Outline each blood parasite and name the species.
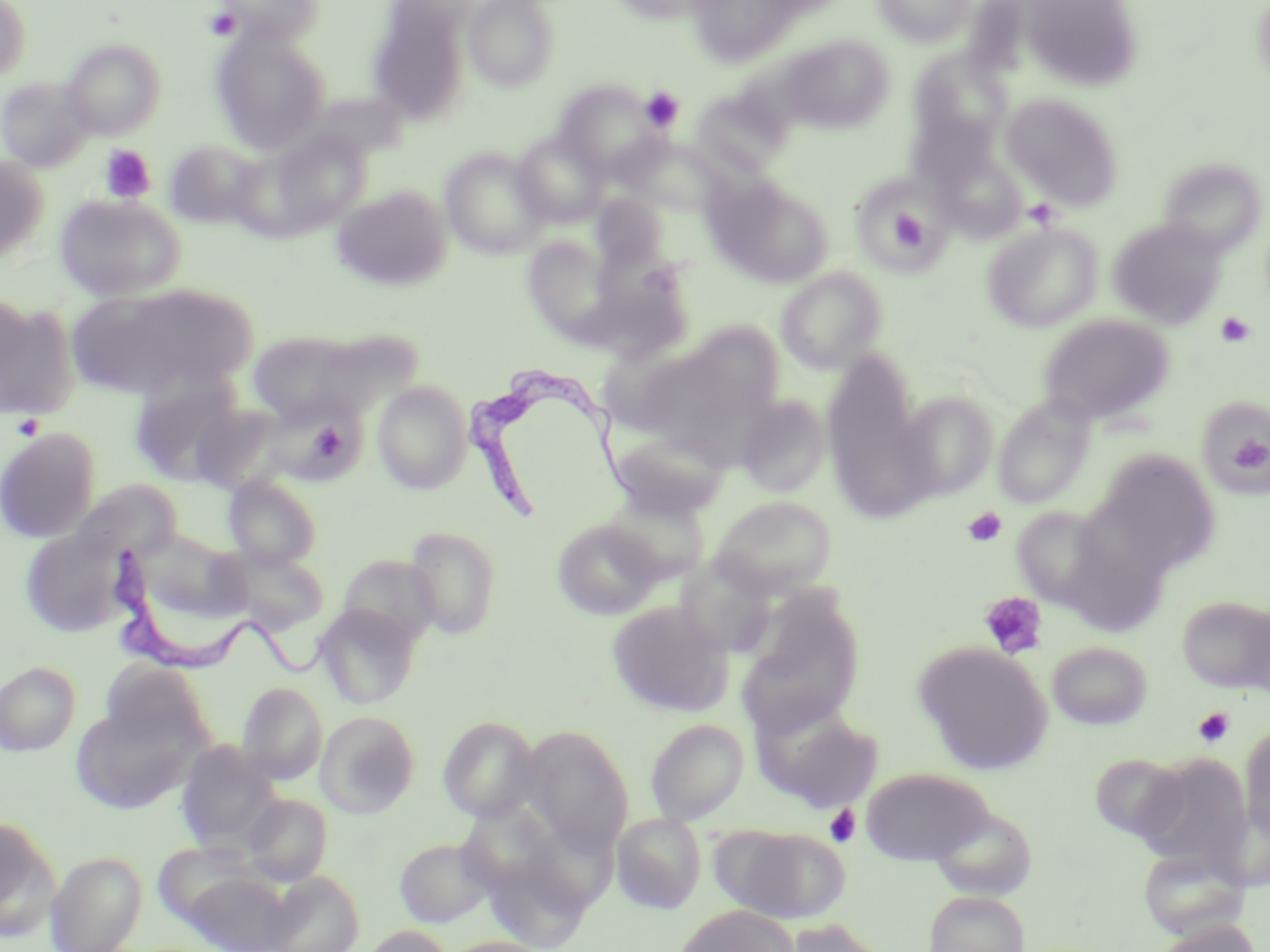
Approximate bounding boxes as (x1, y1, x2, y2) in pixels.
Trypanosoma brucei: (468, 371, 626, 532), (105, 543, 331, 680).
No Plasmodium falciparum, Plasmodium ovale, Plasmodium malariae, Plasmodium vivax, or Babesia divergens observed.

Uninfected red blood cell locations: (216, 0, 324, 45), (464, 0, 560, 91), (606, 0, 721, 26), (686, 0, 810, 67), (872, 0, 977, 47), (1019, 0, 1144, 92), (1251, 0, 1270, 89), (0, 1, 31, 83), (368, 3, 471, 125), (211, 29, 329, 154), (776, 36, 893, 135), (61, 38, 166, 139), (907, 47, 1014, 160), (0, 76, 94, 172), (555, 82, 664, 181), (691, 87, 792, 177), (304, 91, 411, 160), (1001, 92, 1124, 210), (267, 129, 371, 234), (512, 131, 608, 228), (621, 136, 728, 216), (164, 139, 266, 230), (440, 147, 552, 259), (0, 155, 50, 263), (1168, 163, 1262, 256), (705, 175, 832, 287), (332, 186, 452, 291), (591, 193, 670, 270), (53, 194, 185, 301), (1108, 217, 1228, 329), (982, 221, 1102, 333), (522, 233, 622, 344), (776, 267, 887, 374), (69, 282, 253, 401), (0, 295, 78, 420), (1039, 314, 1175, 425), (684, 321, 784, 418), (248, 330, 366, 423), (821, 356, 930, 517), (129, 375, 244, 486), (372, 379, 473, 494), (896, 391, 999, 499), (735, 394, 831, 498), (993, 395, 1095, 510), (1206, 400, 1270, 496), (191, 403, 291, 493), (0, 427, 101, 543), (609, 429, 730, 520), (1093, 451, 1221, 576), (223, 474, 322, 570), (71, 480, 182, 565), (604, 491, 711, 584), (711, 496, 836, 597), (1011, 505, 1113, 608), (552, 518, 664, 620), (404, 525, 503, 639), (19, 528, 135, 638), (132, 529, 251, 630), (218, 545, 329, 634), (337, 553, 441, 649), (676, 554, 778, 658), (1177, 595, 1270, 694), (737, 597, 865, 736), (606, 600, 734, 718), (315, 604, 420, 709), (1046, 641, 1153, 730), (914, 642, 1053, 774), (96, 659, 214, 752), (0, 661, 81, 756), (238, 682, 328, 784), (68, 698, 205, 814), (753, 698, 884, 811), (315, 710, 420, 818), (438, 715, 543, 822), (645, 718, 749, 824), (1239, 722, 1270, 841), (523, 727, 634, 854), (176, 740, 283, 852), (1089, 752, 1190, 844), (1133, 753, 1253, 872), (860, 767, 995, 866), (241, 793, 333, 885), (929, 805, 1038, 901), (612, 813, 706, 914), (0, 815, 60, 937), (720, 825, 849, 924), (393, 836, 495, 927), (1137, 845, 1251, 941), (46, 850, 147, 951), (175, 866, 295, 951), (262, 871, 365, 952), (923, 890, 1030, 952), (675, 904, 798, 952), (776, 918, 891, 952), (1152, 919, 1261, 952), (360, 926, 455, 952). Platelet locations: (205, 7, 241, 41), (640, 87, 684, 132), (99, 145, 156, 203), (865, 191, 942, 260), (888, 209, 928, 251), (1215, 312, 1256, 347), (13, 413, 44, 440), (1225, 425, 1270, 480), (962, 507, 1007, 547), (980, 592, 1048, 659), (1193, 707, 1235, 748), (825, 805, 861, 847). Slide-level diagnosis: Trypanosoma brucei. Single field of view. 1000x magnification. Optical microscopy. Thin blood film. May-Grünwald-Giemsa stain. Image is 1270×952 pixels.